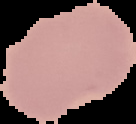

result = negative for malaria parasites
image size = 136×124 pixels
preparation = thin blood smear
image type = segmented cell region with the area outside set to black